Assess this cell for malaria.
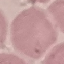

Uninfected.

Summary:
  - Capture: smartphone through the microscope eyepiece
  - Stain: Giemsa
  - Preparation: thin smear
  - Image type: automatically extracted cell patch, resized to 64 × 64 pixels